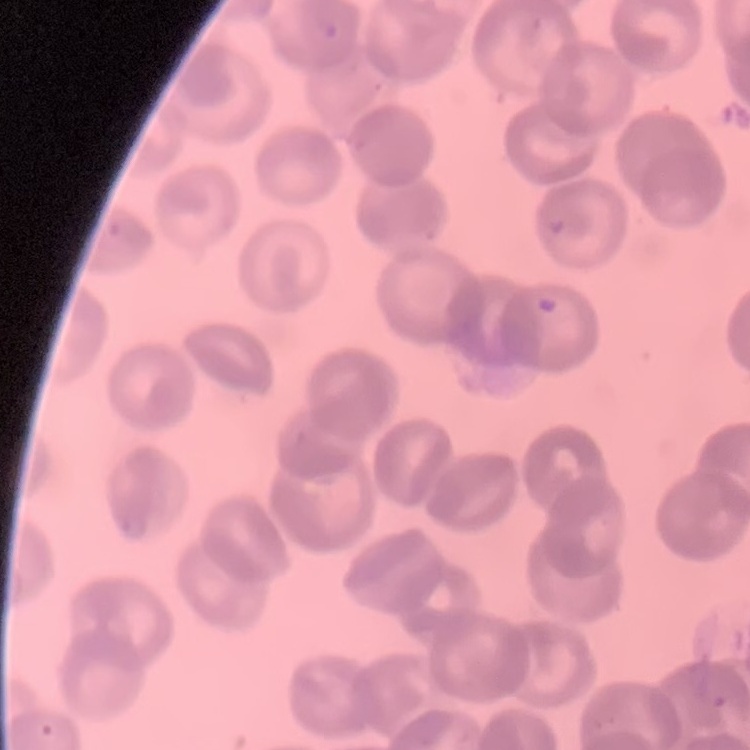

erythrocyte morphology = rouleaux formation
image type = one tile cut from a larger photomicrograph
preparation = thin blood smear
stain = Field's or Giemsa